Report the malaria status of this cell.
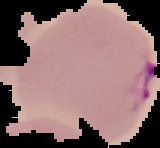

It is parasitized.

Summary:
  - Image type: segmented cell region with the area outside set to black
  - Image size: 160×148 pixels
  - Preparation: thin blood film